State which parasite is depicted.
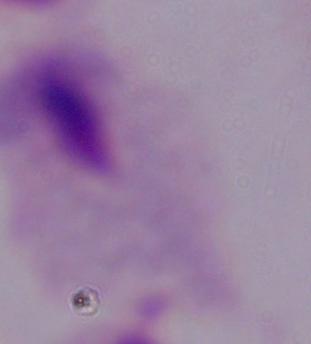

This is a trichomonad.

Summary:
  - Modality: photomicrograph
  - Magnification: 1000x